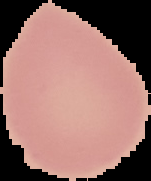
image_type: segmented cell region on a black background
result: no Plasmodium parasites detected
preparation: thin blood smear
image_size: 151×181 pixels